Locate every blood parasite and identify its species.
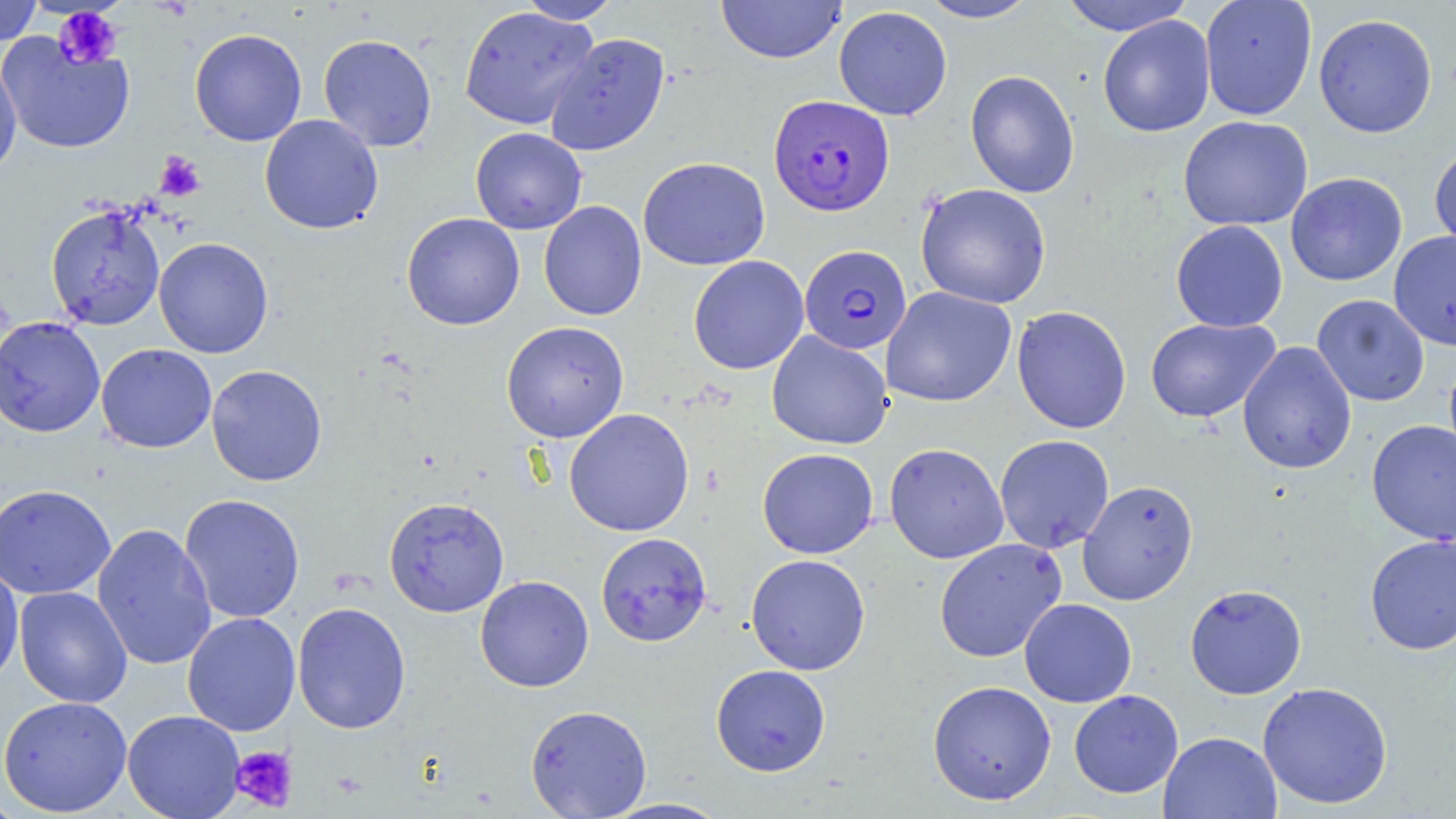

Approximate bounding boxes as (x1, y1, x2, y2) in pixels.
Plasmodium falciparum-infected red blood cells: (768, 94, 894, 216), (798, 246, 912, 354).
No Plasmodium ovale, Plasmodium malariae, Plasmodium vivax, Babesia divergens, or Trypanosoma brucei observed.

slide_level_diagnosis: Plasmodium falciparum
modality: light microscopy
field_of_view: single
magnification: 1000x
stain: May-Grünwald-Giemsa
uninfected_red_blood_cell_locations: 'approximate bounding boxes as (x1, y1, x2, y2) in pixels: (0, 0, 43, 46), (715, 0, 846, 64), (919, 0, 1040, 23), (1058, 0, 1196, 36), (1199, 0, 1317, 120), (517, 1, 621, 25), (458, 6, 599, 130), (833, 6, 952, 121), (1313, 13, 1438, 138), (1097, 15, 1215, 137), (190, 29, 307, 147), (544, 32, 670, 156), (0, 33, 135, 155), (318, 34, 437, 151), (0, 53, 21, 182), (964, 70, 1080, 198), (259, 114, 384, 234), (1178, 115, 1313, 231), (470, 127, 587, 234), (1429, 144, 1456, 255), (638, 156, 770, 271), (1285, 172, 1407, 286), (915, 183, 1051, 309), (538, 201, 647, 321), (45, 203, 166, 330), (401, 212, 525, 331), (1170, 220, 1288, 333), (1388, 231, 1456, 350), (153, 237, 274, 359), (688, 255, 809, 375), (881, 286, 1017, 407), (1312, 294, 1430, 406), (1011, 305, 1132, 434), (0, 316, 105, 438), (1145, 318, 1280, 422), (501, 321, 630, 443), (766, 330, 894, 450), (1237, 341, 1357, 475), (96, 344, 217, 453), (1443, 351, 1456, 471), (206, 365, 327, 486), (563, 408, 695, 537), (1366, 419, 1456, 546), (994, 434, 1114, 553), (884, 442, 1009, 564), (757, 448, 879, 559), (1077, 479, 1199, 605), (0, 483, 116, 599), (179, 493, 305, 623), (383, 496, 510, 617), (92, 522, 217, 671), (595, 532, 712, 646), (1365, 534, 1456, 655), (933, 538, 1067, 663), (745, 554, 871, 675), (0, 561, 24, 690), (475, 575, 594, 692), (1184, 584, 1307, 699), (14, 587, 132, 708), (1019, 598, 1137, 707), (292, 602, 411, 734), (182, 612, 301, 736), (710, 664, 831, 776), (927, 680, 1056, 806), (1257, 681, 1393, 809), (1069, 690, 1183, 798), (0, 695, 132, 816), (524, 704, 652, 817), (122, 710, 246, 819), (1158, 730, 1282, 819), (0, 793, 25, 818), (599, 797, 735, 818)'
preparation: thin blood film
platelet_locations: 'approximate bounding boxes as (x1, y1, x2, y2) in pixels: (53, 6, 123, 69), (155, 151, 206, 201), (230, 745, 297, 812), (332, 771, 367, 799)'
image_size: 1456×819 pixels